Describe the morphology of the red blood cells.
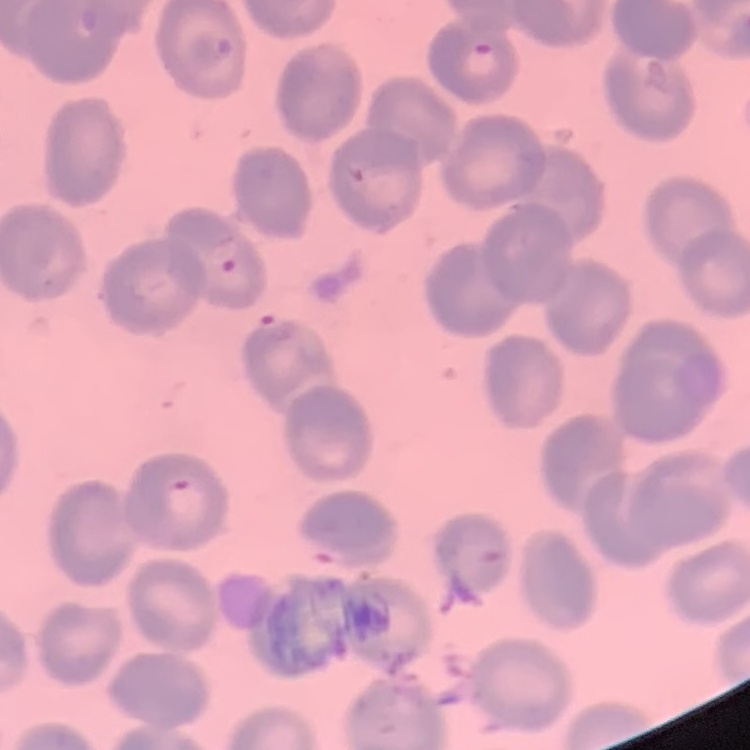
No rouleaux formation.

stain = Field's or Giemsa
preparation = thin blood film
image type = square crop of a larger photomicrograph